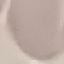 Malaria status: uninfected. Cell patch, automatically extracted from a larger field of view and resized to 64 × 64 pixels. Giemsa-stained preparation. Thin smear of blood. Photographed with a smartphone camera at the microscope eyepiece.